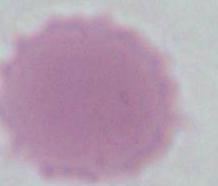
magnification: 1000x
identification: red blood cell
modality: photomicrograph